Assess this cell for malaria.
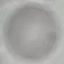
It is uninfected.

Summary:
  - Image type: automatically extracted cell patch, resized to 64 × 64 pixels
  - Capture: smartphone through the microscope eyepiece
  - Preparation: thin blood smear
  - Stain: Giemsa